Locate every Plasmodium falciparum-infected red blood cell.
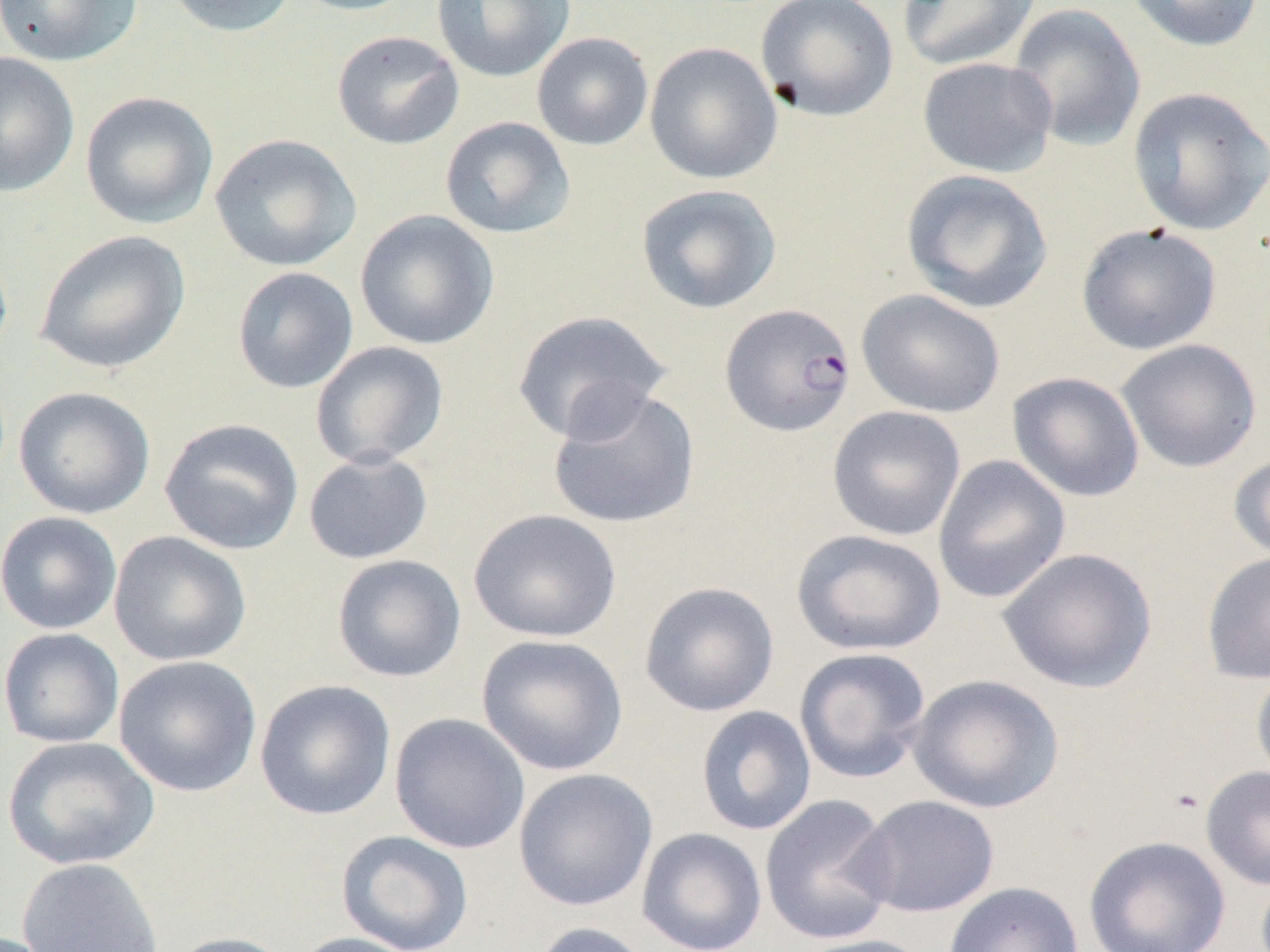
Approximate bounding boxes as named x1/y1/x2/y2 corners in pixels.
Plasmodium falciparum-infected red blood cells: (x1=720, y1=303, x2=856, y2=437).

slide-level diagnosis = Plasmodium falciparum
image size = 1270×952 pixels
magnification = 1000x
preparation = thin blood smear
modality = light microscopy
uninfected red blood cell locations = approximate bounding boxes as named x1/y1/x2/y2 corners in pixels: (x1=0, y1=0, x2=143, y2=67), (x1=164, y1=0, x2=298, y2=38), (x1=287, y1=0, x2=422, y2=17), (x1=431, y1=0, x2=575, y2=83), (x1=755, y1=0, x2=899, y2=122), (x1=897, y1=0, x2=1040, y2=72), (x1=1123, y1=0, x2=1265, y2=53), (x1=1008, y1=3, x2=1146, y2=152), (x1=331, y1=29, x2=464, y2=150), (x1=531, y1=32, x2=654, y2=151), (x1=644, y1=41, x2=783, y2=185), (x1=0, y1=51, x2=80, y2=198), (x1=917, y1=56, x2=1057, y2=178), (x1=1126, y1=86, x2=1269, y2=236), (x1=79, y1=91, x2=218, y2=230), (x1=439, y1=116, x2=577, y2=239), (x1=209, y1=133, x2=362, y2=272), (x1=900, y1=169, x2=1054, y2=313), (x1=635, y1=183, x2=782, y2=315), (x1=354, y1=209, x2=499, y2=351), (x1=1075, y1=223, x2=1222, y2=355), (x1=34, y1=229, x2=191, y2=375), (x1=232, y1=266, x2=359, y2=394), (x1=856, y1=288, x2=1005, y2=418), (x1=509, y1=310, x2=672, y2=444), (x1=1116, y1=338, x2=1262, y2=473), (x1=310, y1=341, x2=450, y2=470), (x1=1007, y1=372, x2=1144, y2=502), (x1=546, y1=384, x2=701, y2=530), (x1=14, y1=386, x2=155, y2=519), (x1=827, y1=405, x2=966, y2=541), (x1=159, y1=417, x2=305, y2=555), (x1=303, y1=450, x2=433, y2=565), (x1=1228, y1=451, x2=1270, y2=564), (x1=932, y1=454, x2=1071, y2=604), (x1=468, y1=509, x2=622, y2=643), (x1=0, y1=511, x2=122, y2=635), (x1=790, y1=528, x2=946, y2=656), (x1=108, y1=530, x2=252, y2=666), (x1=997, y1=547, x2=1158, y2=694), (x1=1201, y1=550, x2=1270, y2=685), (x1=332, y1=553, x2=467, y2=683), (x1=638, y1=581, x2=780, y2=717), (x1=0, y1=627, x2=124, y2=748), (x1=476, y1=634, x2=628, y2=776), (x1=793, y1=647, x2=932, y2=784), (x1=114, y1=654, x2=262, y2=797), (x1=1251, y1=664, x2=1270, y2=790), (x1=908, y1=674, x2=1065, y2=814), (x1=254, y1=678, x2=396, y2=821), (x1=695, y1=706, x2=817, y2=836), (x1=389, y1=712, x2=530, y2=854), (x1=1, y1=736, x2=160, y2=871), (x1=1201, y1=765, x2=1270, y2=891), (x1=512, y1=767, x2=658, y2=912), (x1=760, y1=794, x2=898, y2=945), (x1=852, y1=795, x2=1000, y2=918), (x1=637, y1=827, x2=767, y2=952), (x1=336, y1=830, x2=474, y2=952), (x1=1083, y1=835, x2=1231, y2=952), (x1=16, y1=856, x2=164, y2=951), (x1=942, y1=881, x2=1084, y2=952), (x1=530, y1=921, x2=657, y2=952), (x1=165, y1=931, x2=298, y2=952), (x1=288, y1=931, x2=426, y2=952), (x1=790, y1=934, x2=935, y2=952)
field of view = one of a larger specimen